Classify this cell by malaria status.
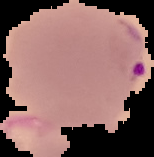
It is parasitized.

Summary:
  - Image type: cell region segmented out of the field of view; surrounding area masked to black
  - Preparation: thin blood film
  - Image size: 154×157 pixels